Point out each leukocyte.
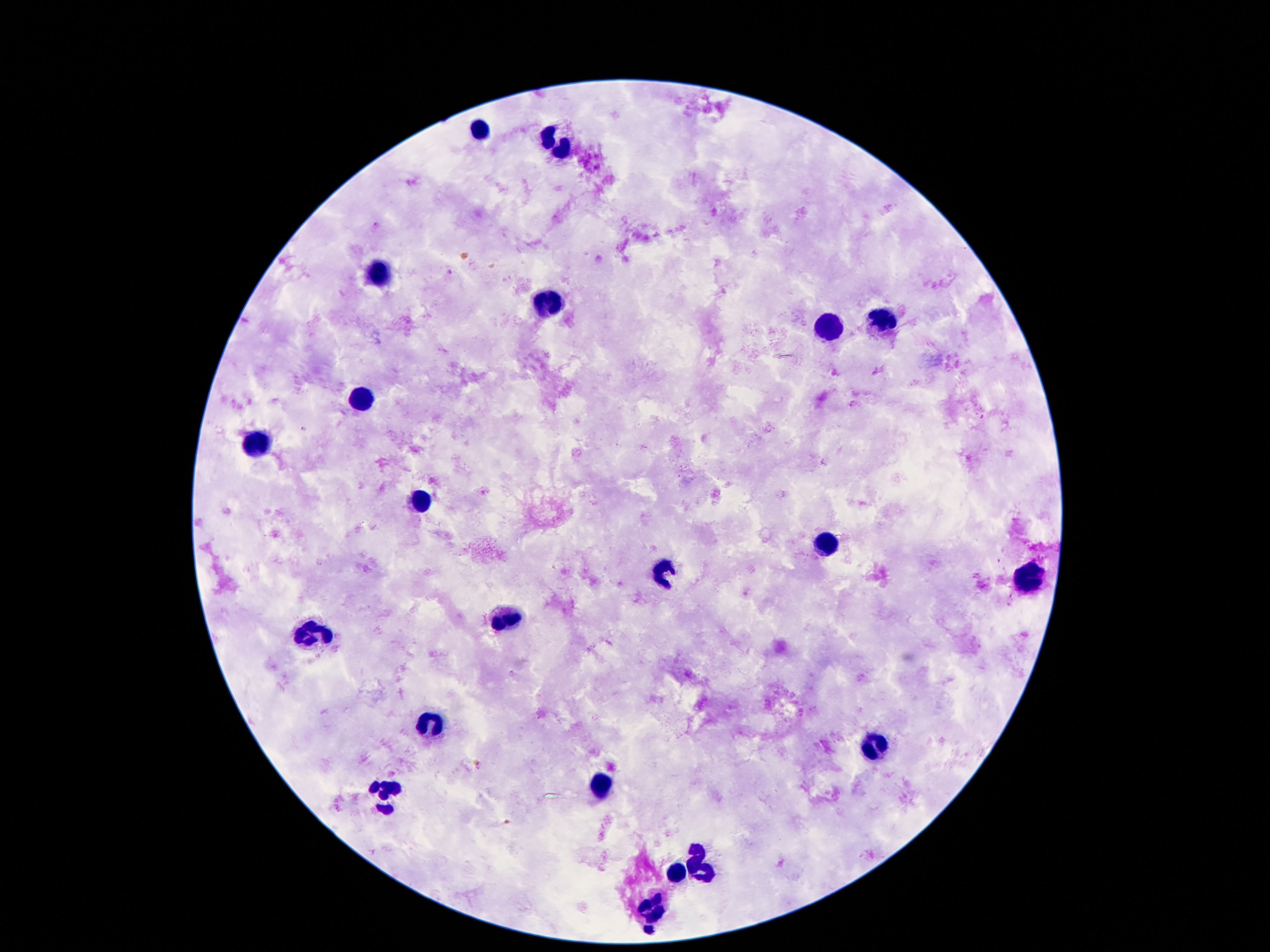

Approximate object centers, in pixels from the top-left corner.
Leukocytes: (x=477, y=127), (x=559, y=141), (x=377, y=276), (x=549, y=304), (x=879, y=317), (x=828, y=328), (x=361, y=397), (x=256, y=444), (x=420, y=500), (x=828, y=543), (x=666, y=569), (x=1033, y=577), (x=504, y=620), (x=313, y=633), (x=432, y=723), (x=879, y=747), (x=600, y=788), (x=383, y=798), (x=703, y=862), (x=678, y=874), (x=651, y=909).

One field from this slide. Giemsa-stained preparation. Thick peripheral-blood smear. Photographed through the microscope eyepiece with a smartphone camera. Patient malaria status: not infected. 100x magnification. Image is 1270×952 pixels.